Locate and identify every blood parasite.
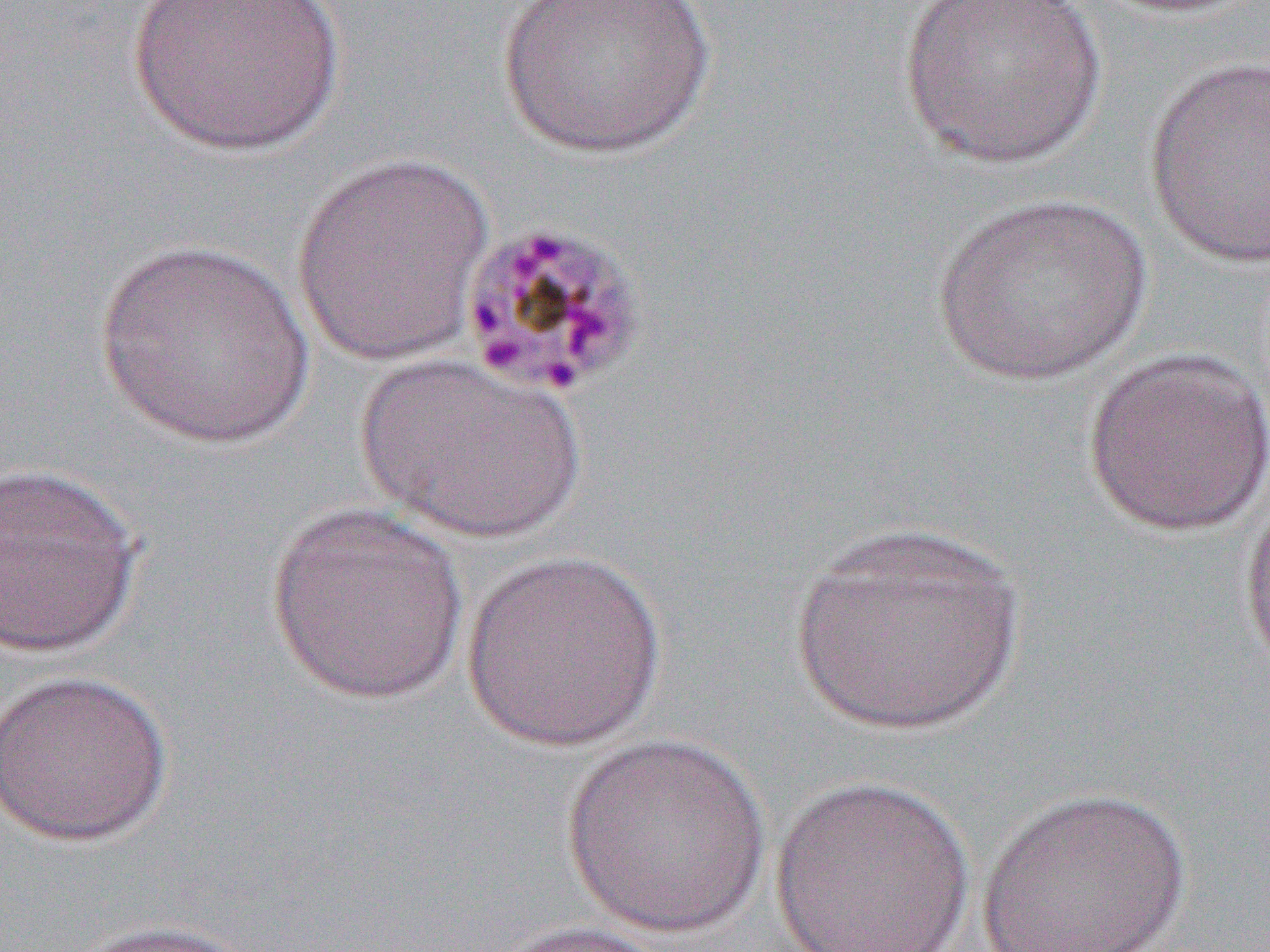

Approximate bounding boxes as named x1/y1/x2/y2 corners in pixels.
Plasmodium malariae-infected red blood cells: (x1=455, y1=216, x2=647, y2=398).
No Plasmodium falciparum, Plasmodium ovale, Plasmodium vivax, Babesia divergens, or Trypanosoma brucei observed.

Uninfected red blood cell locations: (x1=126, y1=0, x2=347, y2=157), (x1=496, y1=0, x2=716, y2=160), (x1=895, y1=0, x2=1110, y2=170), (x1=1143, y1=55, x2=1270, y2=269), (x1=290, y1=150, x2=496, y2=369), (x1=930, y1=192, x2=1154, y2=388), (x1=93, y1=240, x2=317, y2=451), (x1=1080, y1=346, x2=1269, y2=537), (x1=354, y1=352, x2=585, y2=545), (x1=0, y1=460, x2=145, y2=660), (x1=1237, y1=466, x2=1270, y2=688), (x1=265, y1=502, x2=472, y2=705), (x1=782, y1=521, x2=1031, y2=740), (x1=460, y1=549, x2=669, y2=751), (x1=0, y1=668, x2=174, y2=847), (x1=559, y1=732, x2=774, y2=938), (x1=770, y1=774, x2=975, y2=950), (x1=975, y1=785, x2=1194, y2=952), (x1=63, y1=918, x2=265, y2=952), (x1=480, y1=919, x2=676, y2=952). Slide-level diagnosis: Plasmodium malariae. Image is 1270×952 pixels. One field of a larger specimen. Light microscopy. Thin blood film. 1000x magnification.